Locate platelets.
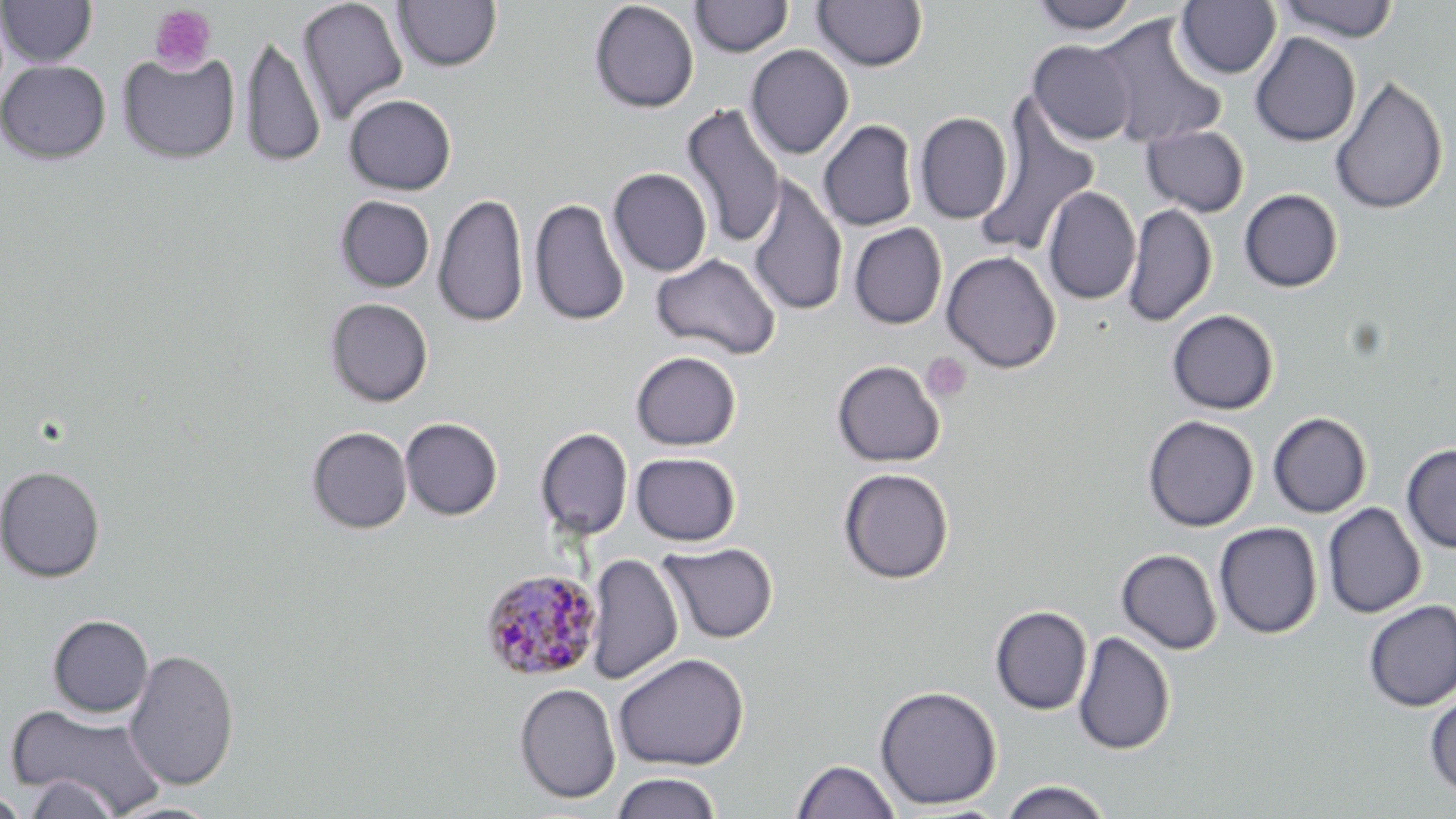
Approximate bounding boxes as [x1, y1, x2, y2] in pixels.
Platelets: [149, 4, 217, 74], [921, 352, 972, 402].

Uninfected red blood cell locations: [0, 0, 97, 67], [296, 0, 409, 124], [393, 0, 501, 72], [690, 0, 792, 57], [813, 0, 927, 71], [1028, 0, 1141, 34], [1276, 0, 1400, 42], [589, 1, 699, 113], [1176, 1, 1281, 79], [1091, 13, 1228, 150], [1250, 32, 1361, 147], [240, 33, 326, 169], [1028, 39, 1136, 145], [745, 45, 854, 160], [117, 50, 240, 164], [0, 60, 111, 164], [1329, 75, 1449, 215], [343, 94, 456, 195], [681, 102, 787, 248], [975, 103, 1101, 257], [914, 112, 1013, 224], [818, 119, 919, 231], [1141, 124, 1249, 217], [607, 168, 712, 277], [747, 175, 848, 317], [1042, 186, 1141, 305], [1239, 189, 1344, 292], [433, 192, 529, 329], [335, 195, 434, 292], [529, 196, 630, 327], [1123, 203, 1216, 328], [848, 222, 947, 329], [941, 250, 1061, 373], [651, 252, 781, 360], [325, 297, 434, 407], [1166, 309, 1279, 415], [630, 351, 743, 451], [832, 360, 945, 467], [1267, 412, 1372, 518], [1142, 415, 1259, 532], [400, 417, 503, 520], [306, 426, 412, 534], [536, 428, 633, 540], [1401, 444, 1456, 553], [630, 452, 742, 546], [0, 465, 105, 582], [838, 467, 954, 584], [1323, 502, 1426, 619], [1214, 522, 1322, 639], [660, 542, 777, 643], [1116, 548, 1223, 654], [586, 553, 683, 684], [1362, 600, 1456, 712], [990, 606, 1092, 715], [47, 614, 154, 718], [1072, 631, 1176, 756], [122, 648, 240, 790], [613, 652, 749, 771], [514, 682, 621, 804], [874, 684, 1002, 810], [1425, 689, 1456, 799], [6, 701, 168, 816], [792, 758, 901, 819], [610, 771, 723, 819], [21, 774, 123, 819], [1000, 780, 1113, 819], [0, 790, 30, 818], [109, 802, 224, 819]. Plasmodium malariae-infected red blood cell locations: [478, 568, 602, 682]. Slide-level diagnosis: Plasmodium malariae. 1000x magnification. Image is 1456×819 pixels. Thin blood film. Light microscopy. May-Grünwald-Giemsa stain. One field of a larger specimen.